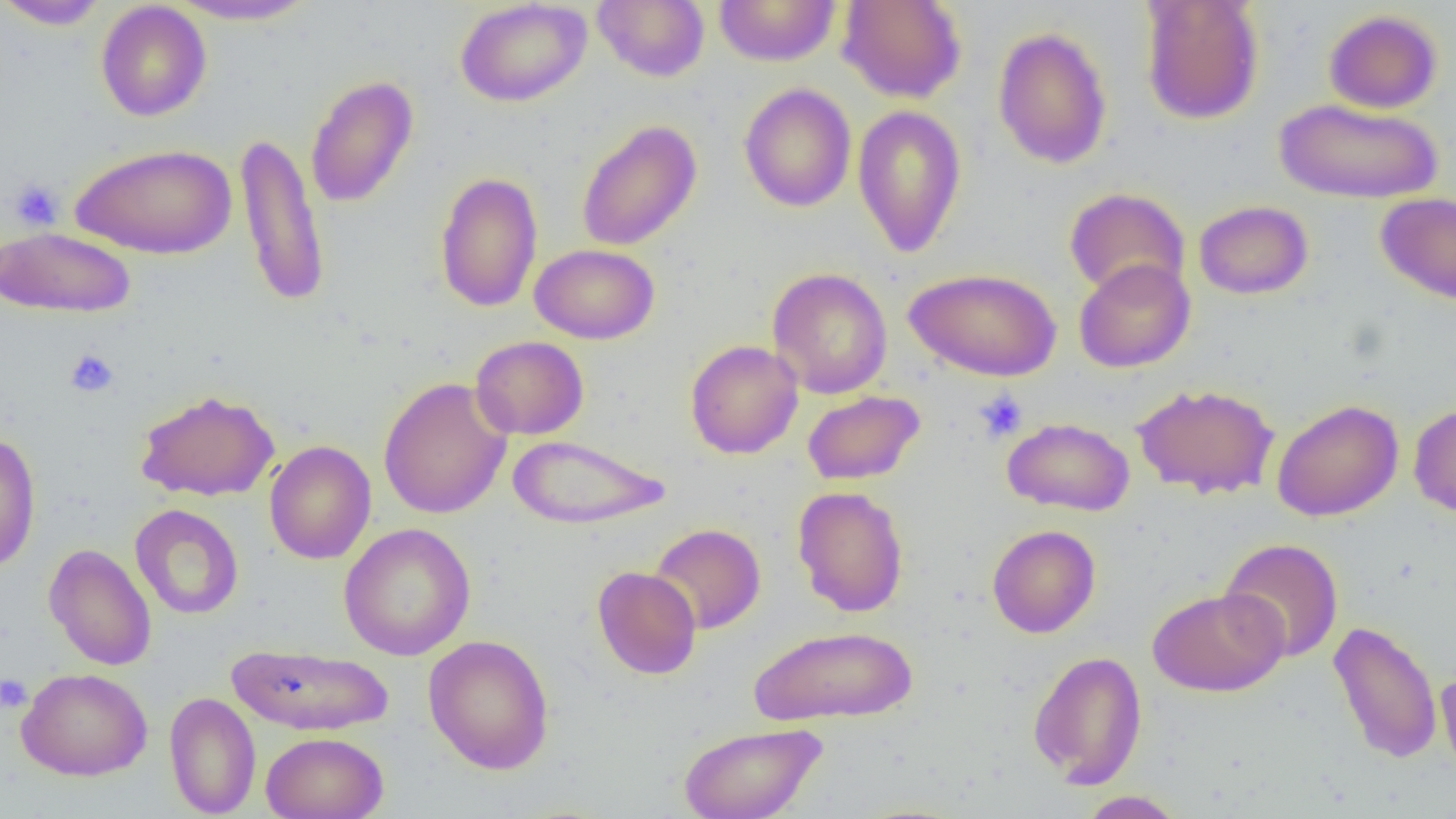

Summary:
  - Coordinate format: approximate bounding boxes as [x1, y1, x2, y2] in pixels
  - Uninfected red blood cell locations: [0, 0, 110, 30], [167, 0, 320, 26], [455, 0, 592, 107], [593, 0, 710, 82], [713, 0, 842, 66], [836, 0, 967, 103], [1139, 1, 1265, 126], [95, 2, 212, 122], [1323, 9, 1443, 113], [993, 26, 1112, 169], [305, 75, 419, 208], [739, 83, 856, 212], [1274, 98, 1443, 204], [852, 104, 967, 257], [576, 120, 702, 251], [236, 132, 330, 309], [70, 142, 237, 259], [434, 170, 543, 313], [1064, 187, 1190, 299], [1376, 192, 1456, 305], [1193, 200, 1313, 300], [1, 226, 137, 318], [530, 244, 660, 344], [1073, 258, 1195, 373], [767, 267, 893, 398], [904, 267, 1062, 381], [470, 335, 589, 440], [685, 340, 803, 459], [378, 376, 513, 520], [1132, 382, 1280, 500], [135, 389, 280, 501], [802, 390, 925, 485], [1271, 399, 1404, 522], [1408, 403, 1456, 518], [1002, 417, 1135, 516], [0, 431, 41, 573], [508, 433, 671, 529], [263, 440, 376, 565], [793, 486, 909, 617], [130, 504, 244, 620], [338, 523, 476, 661], [649, 523, 766, 635], [987, 524, 1101, 638], [1218, 538, 1344, 663], [44, 543, 156, 671], [592, 566, 702, 680], [1148, 587, 1287, 697], [1328, 620, 1442, 765], [749, 624, 918, 727], [423, 634, 555, 774], [227, 643, 395, 736], [1028, 650, 1147, 788], [16, 667, 153, 781], [1436, 671, 1456, 783], [164, 691, 261, 818], [678, 721, 827, 819], [261, 732, 389, 819], [1077, 790, 1185, 818]
  - Platelet locations: [8, 179, 64, 231], [64, 348, 119, 398], [974, 390, 1028, 443], [0, 673, 33, 713]
  - Slide-level diagnosis: no evidence of blood parasites
  - Field of view: single
  - Modality: optical microscopy
  - Image size: 1456×819 pixels
  - Preparation: thin blood smear
  - Magnification: 1000x